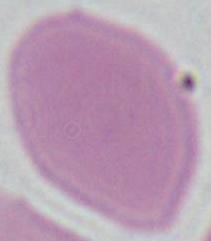 Micrograph. A red blood cell is shown. 1000x magnification.